Assess this cell for malaria.
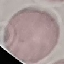

It is uninfected.

Cell patch, automatically extracted from a larger field of view and resized to 64 × 64 pixels. Thin blood film. Giemsa-stained preparation. Acquired by smartphone through the microscope eyepiece.